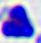

modality = photomicrograph
identification = white blood cell
magnification = 400x